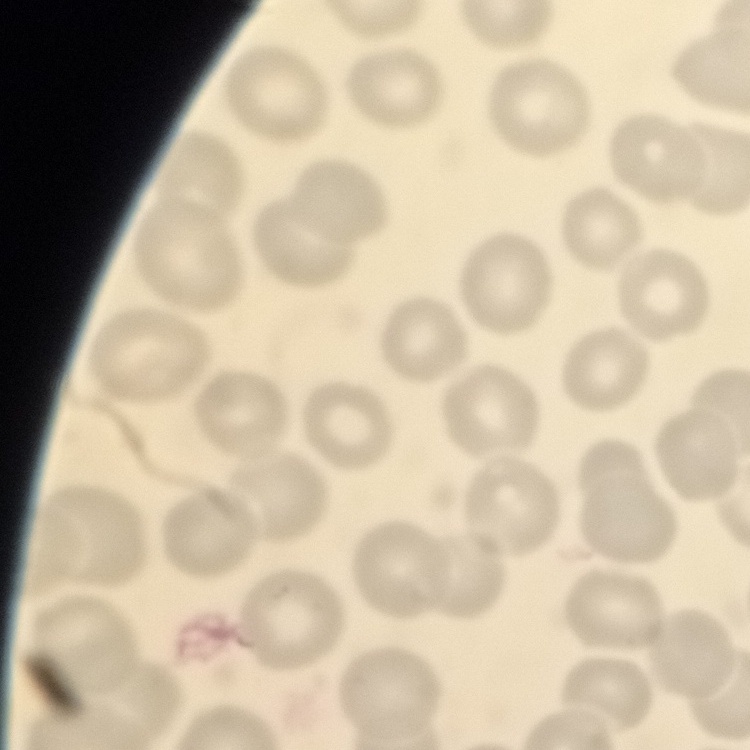

red blood cell morphology = no rouleaux formation
image type = one tile cut from a larger photomicrograph
preparation = thin peripheral smear
stain = Field's or Giemsa